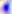

Summary:
  - Identification: Toxoplasma gondii
  - Magnification: 400x
  - Modality: photomicrograph